Identify the parasite.
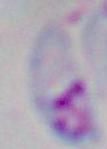

This is Toxoplasma gondii.

magnification: 1000x
modality: photomicrograph